Name the parasite shown.
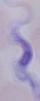
A trypanosome.

Photomicrograph. Captured at 1000x magnification.